Classify this cell by malaria status.
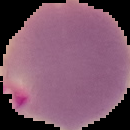

It is parasitized.

Summary:
  - Preparation: thin blood smear
  - Image type: segmented cell region with the area outside set to black
  - Image size: 130×130 pixels